Identify the parasite.
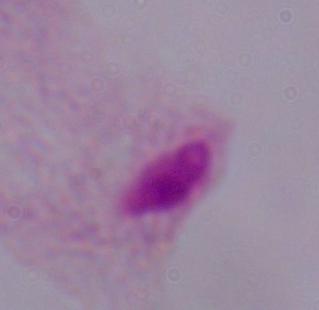

A trichomonad.

Micrograph. 1000x magnification.